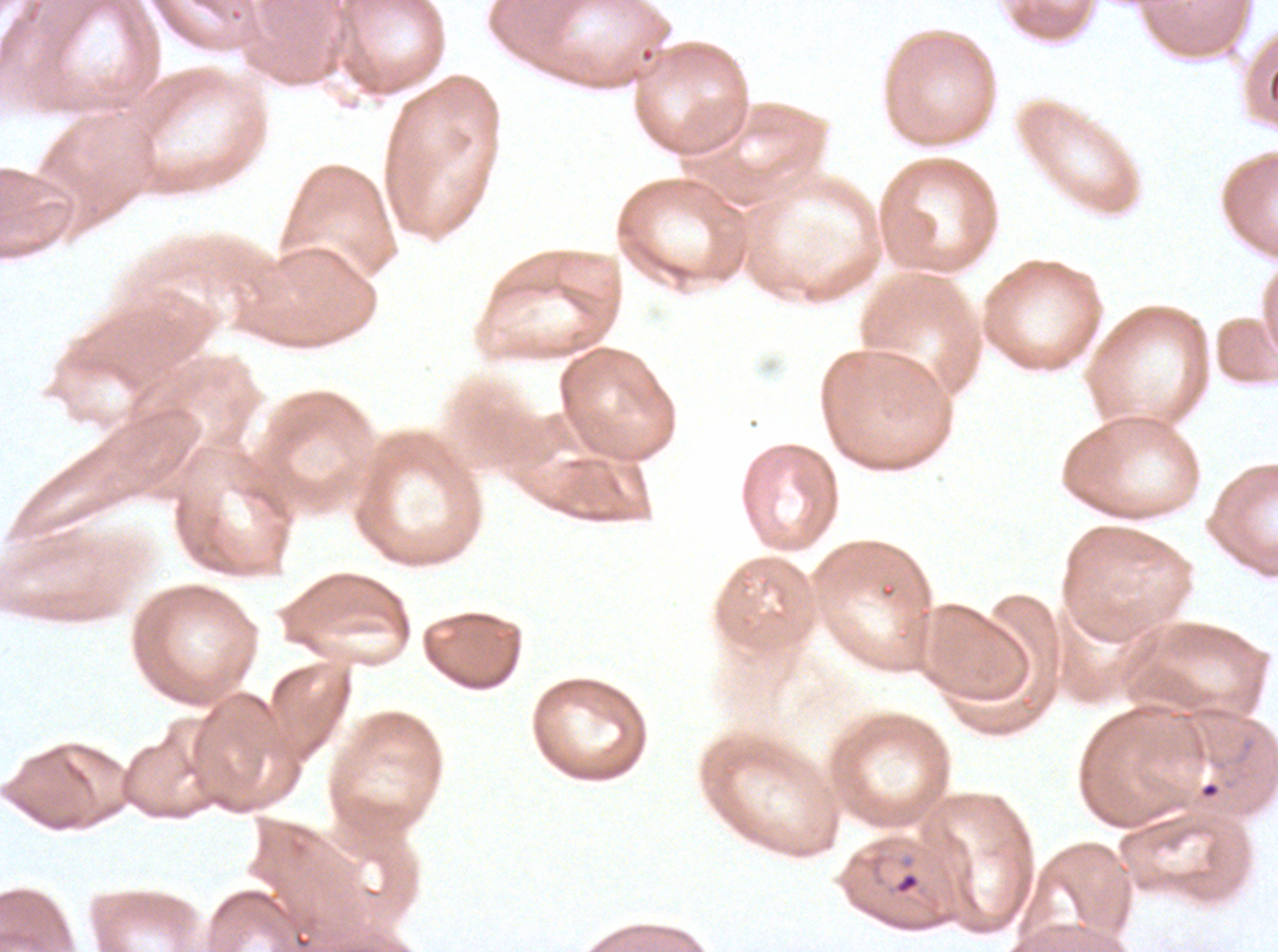
{
  "debris_locations": "approximate bounding boxes as (x1, y1, x2, y2) in pixels: (1198, 780, 1221, 799)",
  "ring_locations": "approximate bounding boxes as (x1, y1, x2, y2) in pixels: (895, 873, 919, 894)",
  "field_of_view": "one sub-image of a larger composite",
  "image_size": "1278×952 pixels",
  "specimen": "Plasmodium falciparum cultured ex vivo for 24 to 48 hours, from a patient in The Gambia",
  "stain": "Giemsa",
  "preparation": "thin blood film"
}